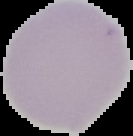

Summary:
  - Image type: cell region segmented out of the field of view; surrounding area masked to black
  - Result: negative for malaria parasites
  - Image size: 133×136 pixels
  - Preparation: thin blood smear